Report the malaria status of this cell.
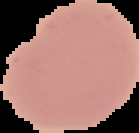

Uninfected.

{
  "preparation": "thin blood film",
  "image_size": "139×133 pixels",
  "image_type": "cell region segmented out of the field of view; surrounding area masked to black"
}